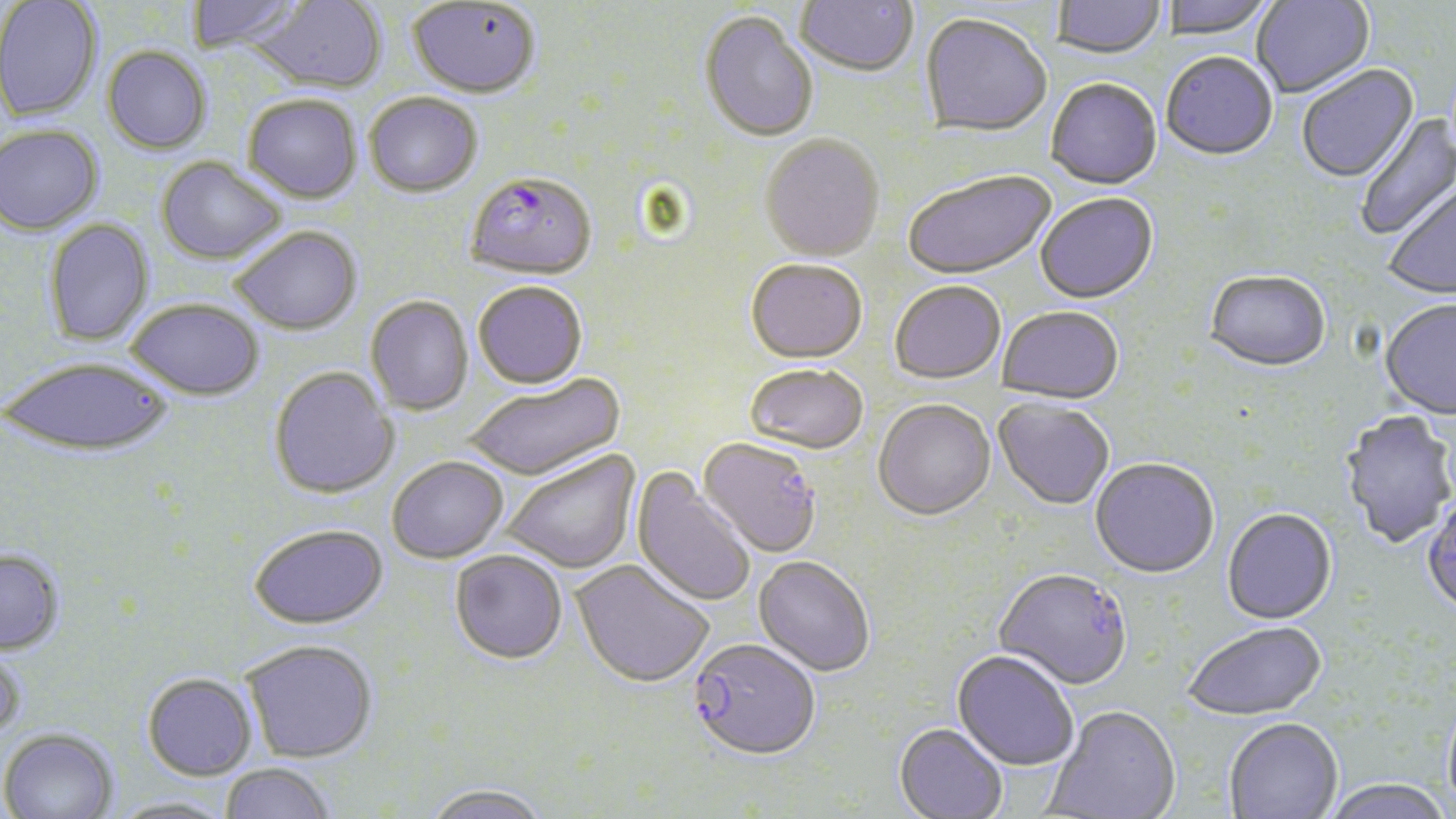
slide_level_diagnosis: Plasmodium falciparum
magnification: 1000x
stain: May-Grünwald-Giemsa
plasmodium_falciparum_infected_red_blood_cell_locations: 'approximate bounding boxes as (x1,y1)-(x2,y2) corner pairs in pixels: (465,175)-(596,284), (688,641)-(821,763)'
uninfected_red_blood_cell_locations: 'approximate bounding boxes as (x1,y1)-(x2,y2) corner pairs in pixels: (186,0)-(305,54), (248,0)-(387,96), (795,0)-(919,80), (1162,0)-(1275,41), (1252,0)-(1374,100), (0,1)-(102,122), (1052,1)-(1165,61), (407,2)-(540,101), (699,13)-(819,145), (920,16)-(1052,139), (101,47)-(212,155), (1161,55)-(1278,163), (1297,65)-(1420,184), (1045,80)-(1163,192), (243,95)-(362,205), (364,95)-(484,200), (1354,113)-(1456,242), (0,124)-(103,235), (759,137)-(884,264), (156,156)-(288,266), (903,171)-(1056,282), (1382,183)-(1456,301), (1036,195)-(1158,306), (43,218)-(154,348), (230,227)-(362,337), (745,262)-(868,366), (1204,272)-(1331,375), (473,283)-(588,391), (890,283)-(1006,386), (365,297)-(474,417), (127,298)-(264,400), (1380,301)-(1456,420), (998,308)-(1124,406), (2,356)-(172,456), (743,366)-(868,457), (269,367)-(400,499), (463,376)-(626,484), (993,400)-(1114,511), (873,402)-(996,524), (1340,412)-(1456,549), (697,438)-(822,559), (501,449)-(642,575), (387,456)-(509,563), (1090,460)-(1219,580), (631,467)-(756,609), (1422,496)-(1456,619), (1222,509)-(1337,626), (249,523)-(389,629), (0,549)-(65,655), (449,551)-(568,666), (753,557)-(874,678), (570,561)-(714,690), (993,570)-(1132,692), (1183,622)-(1327,722), (241,639)-(378,762), (0,640)-(27,741), (952,651)-(1079,772), (142,672)-(258,780), (1442,695)-(1456,819), (1043,707)-(1180,818), (1224,718)-(1343,819), (894,724)-(1008,819), (0,727)-(119,819), (219,762)-(338,819), (1323,779)-(1453,819), (420,784)-(554,819), (108,795)-(237,819)'
image_size: 1456×819 pixels
preparation: thin blood film
modality: light microscopy
field_of_view: single